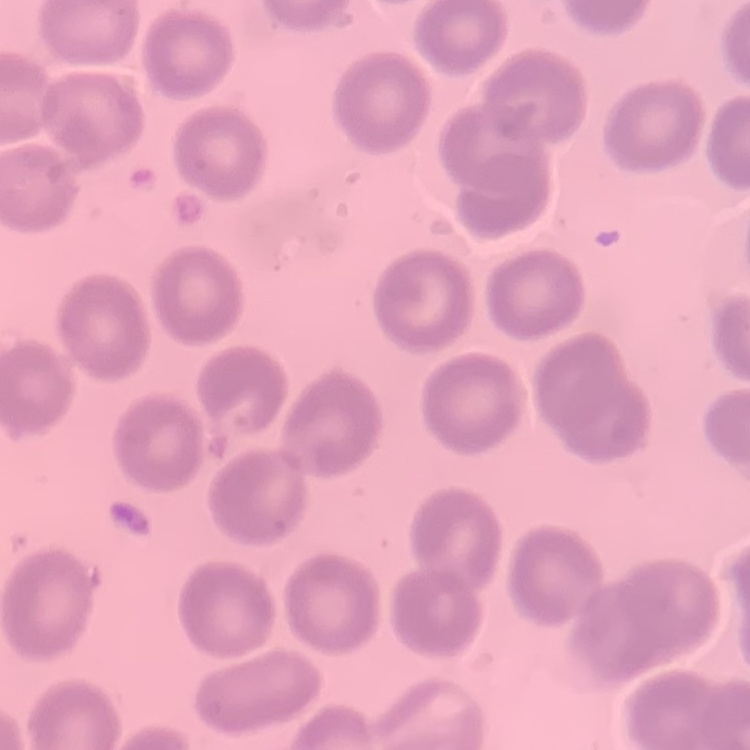

Summary:
  - Red blood cell morphology: no rouleaux formation
  - Stain: Field's or Giemsa
  - Preparation: thin blood smear
  - Image type: square crop of a larger photomicrograph